Assess for Plasmodium parasites.
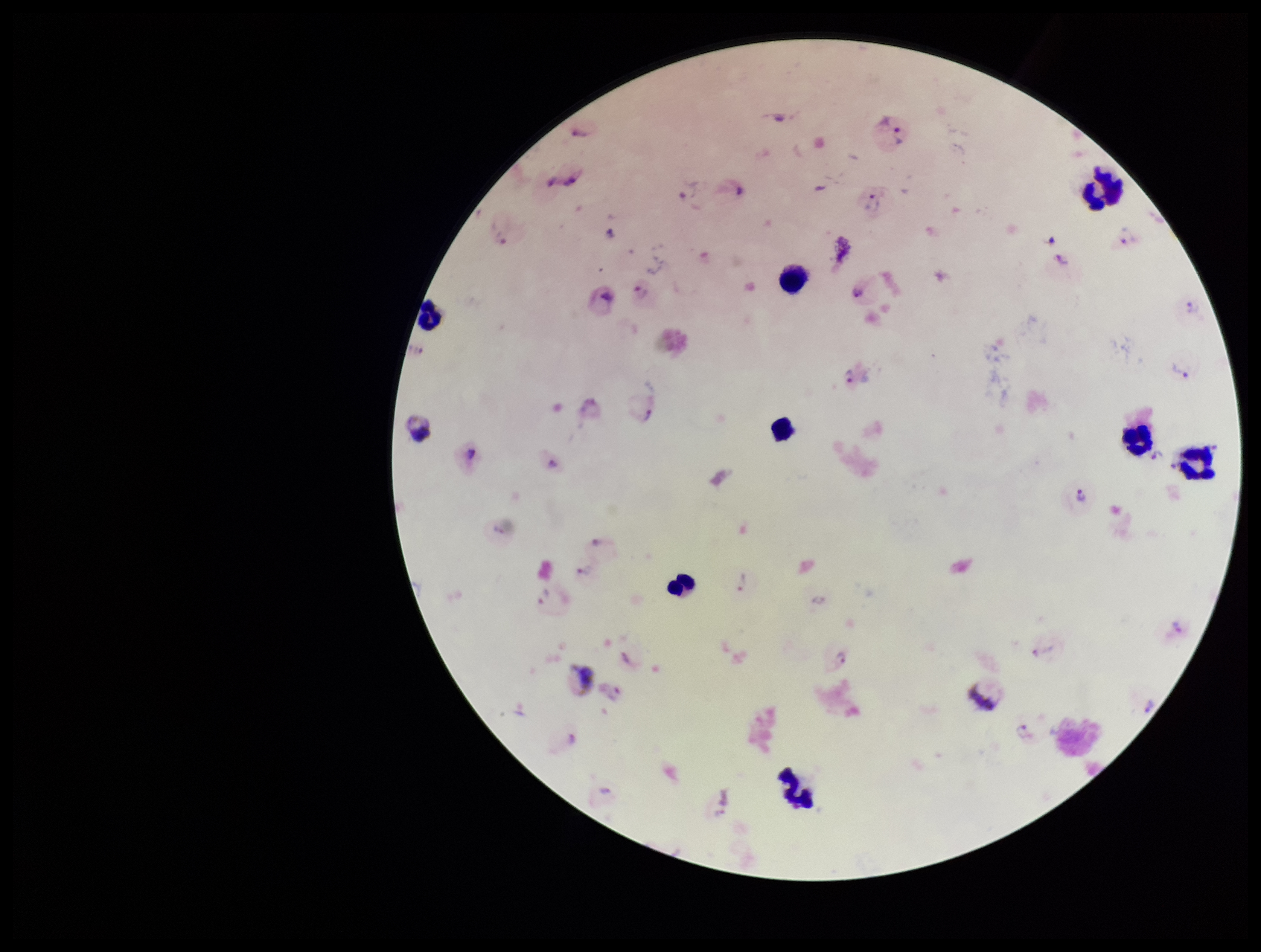

Identified.

stain = Giemsa
leukocyte count = 9
patient malaria status = infected
image size = 1261×952 pixels
preparation = thick smear
capture = smartphone photograph through the microscope eyepiece
field of view = one from this slide
parasite count = 28
species reported for this patient = Plasmodium vivax